Locate every blood parasite and identify its species.
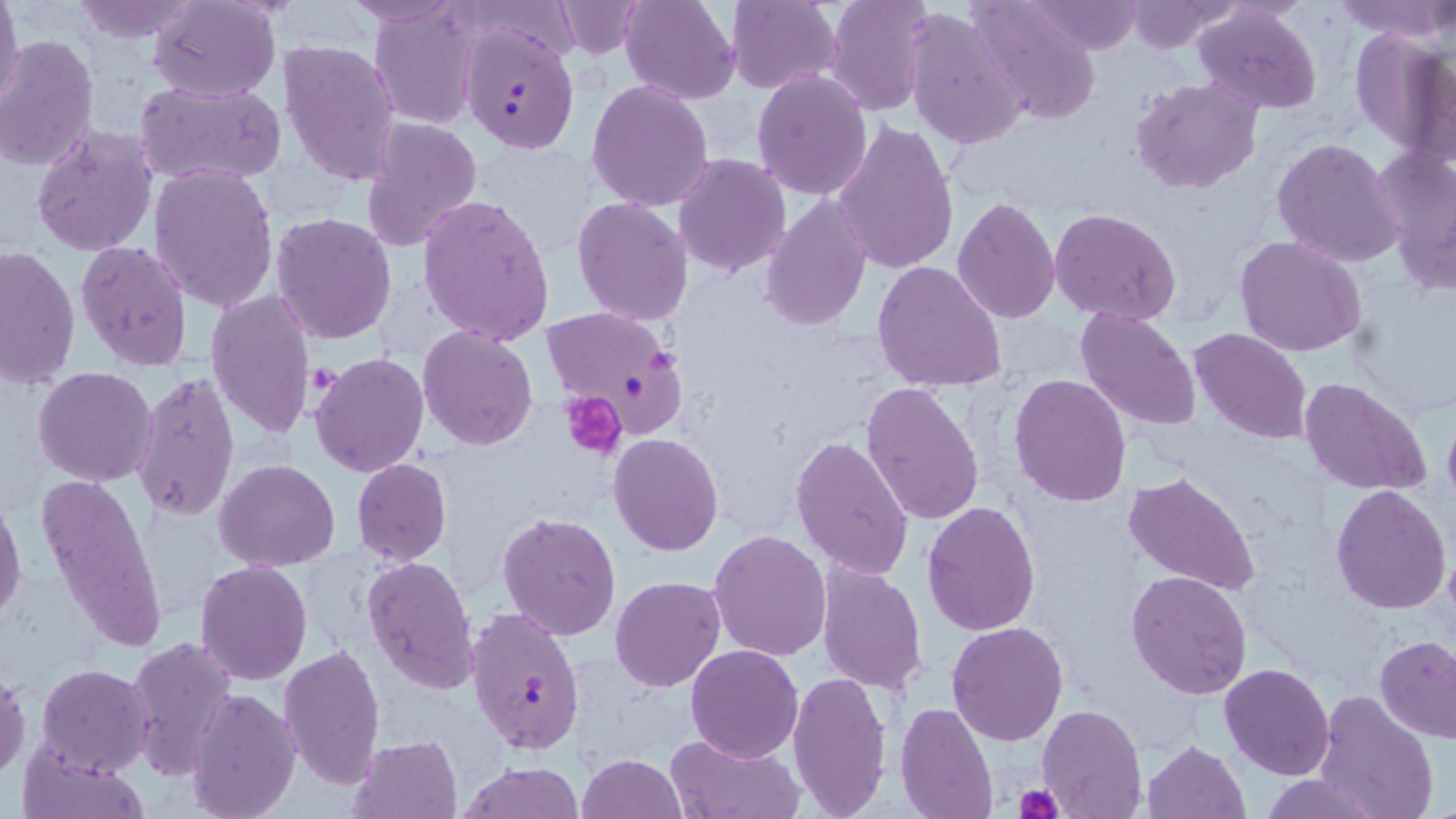

Approximate bounding boxes as [x1, y1, x2, y2] in pixels.
Plasmodium falciparum-infected red blood cells: [460, 25, 579, 153], [538, 306, 688, 430], [464, 605, 587, 753].
No Plasmodium ovale, Plasmodium malariae, Plasmodium vivax, Babesia divergens, or Trypanosoma brucei observed.

Uninfected red blood cell locations: [0, 0, 24, 112], [341, 0, 464, 27], [553, 0, 649, 59], [619, 0, 741, 104], [724, 0, 841, 92], [826, 0, 935, 116], [1023, 0, 1148, 56], [1332, 0, 1451, 44], [71, 1, 202, 43], [148, 1, 281, 101], [965, 1, 1103, 126], [1124, 1, 1237, 54], [370, 3, 483, 131], [1193, 4, 1322, 114], [903, 7, 1026, 151], [1349, 28, 1455, 161], [0, 35, 98, 175], [278, 38, 400, 186], [751, 69, 874, 200], [1131, 77, 1261, 194], [136, 79, 287, 186], [586, 80, 713, 213], [360, 116, 484, 254], [831, 120, 960, 275], [31, 126, 159, 256], [1272, 138, 1403, 267], [1371, 145, 1456, 287], [674, 152, 791, 277], [147, 162, 278, 311], [416, 194, 555, 347], [759, 195, 872, 332], [570, 196, 694, 325], [951, 197, 1062, 324], [1049, 207, 1182, 328], [271, 212, 398, 344], [1234, 235, 1367, 357], [76, 240, 194, 371], [0, 244, 80, 391], [871, 260, 1008, 393], [206, 287, 316, 441], [1075, 305, 1202, 432], [419, 326, 537, 449], [1188, 327, 1314, 445], [311, 353, 430, 477], [33, 366, 158, 486], [131, 370, 240, 524], [1008, 373, 1133, 507], [1300, 376, 1433, 496], [861, 381, 985, 527], [1441, 412, 1456, 509], [608, 433, 724, 556], [791, 435, 913, 582], [216, 459, 340, 570], [352, 459, 453, 565], [1122, 470, 1262, 596], [36, 472, 168, 657], [1331, 484, 1451, 613], [0, 494, 24, 625], [920, 499, 1040, 636], [497, 513, 622, 641], [709, 531, 832, 662], [362, 554, 480, 694], [815, 559, 927, 695], [194, 560, 313, 685], [1126, 568, 1253, 700], [610, 575, 725, 691], [946, 621, 1069, 746], [1376, 634, 1456, 741], [123, 636, 240, 781], [279, 642, 387, 789], [685, 644, 803, 762], [35, 662, 154, 777], [1219, 663, 1334, 781], [0, 669, 29, 781], [786, 670, 894, 818], [187, 685, 300, 819], [1313, 691, 1440, 819], [896, 701, 1000, 818], [1037, 704, 1147, 818], [665, 730, 803, 818], [345, 733, 464, 819], [1142, 740, 1251, 818], [17, 745, 150, 819], [577, 752, 689, 819], [459, 760, 585, 818], [1263, 773, 1381, 818]. Platelet locations: [308, 363, 338, 401], [562, 390, 626, 459], [1013, 786, 1064, 819]. Slide-level diagnosis: Plasmodium falciparum. 1000x magnification. Image is 1456×819 pixels. May-Grünwald-Giemsa-stained preparation. Thin blood smear. Single field of view. Optical microscopy.